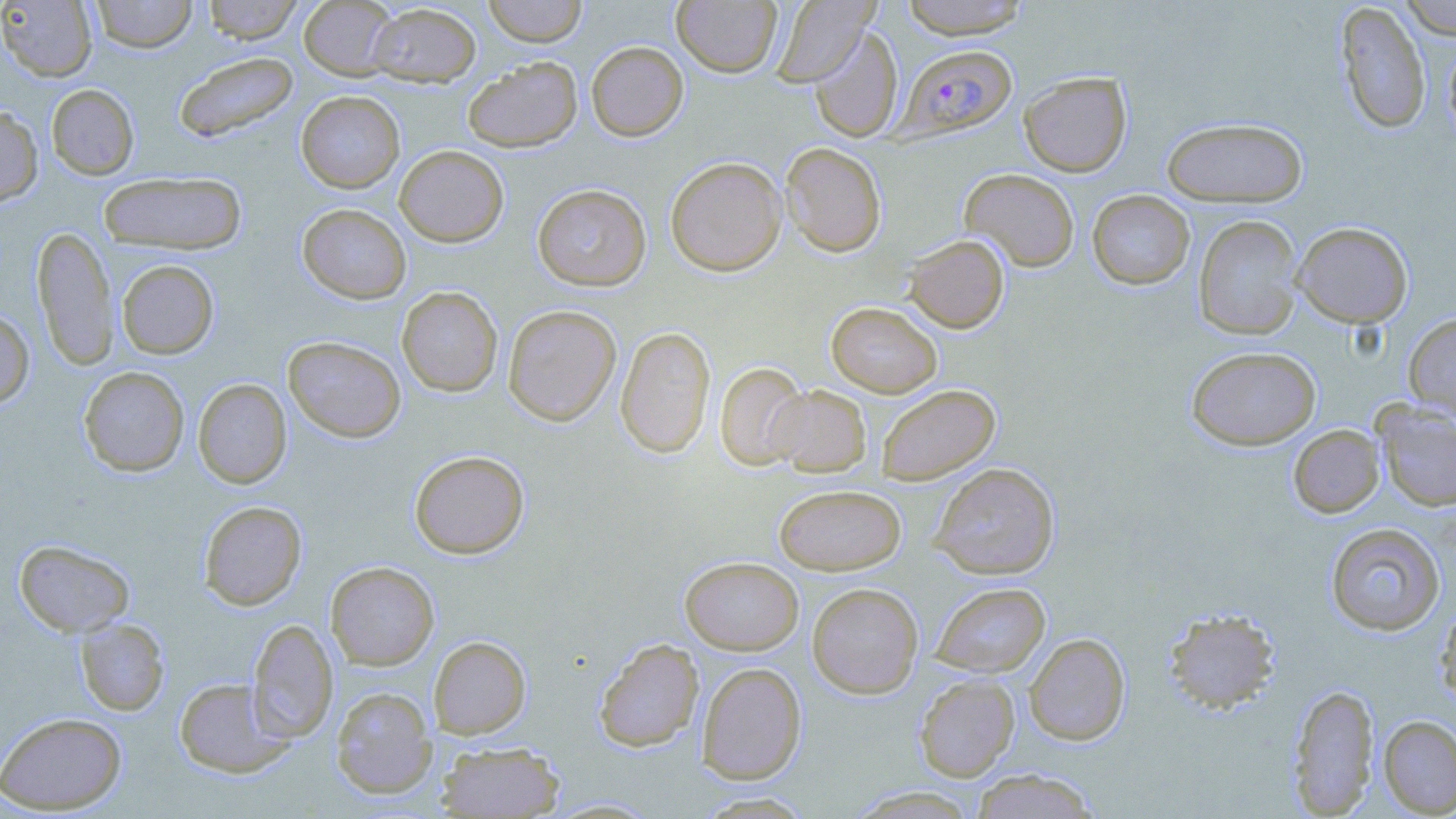
plasmodium_falciparum_infected_red_blood_cell_locations: 'approximate bounding boxes as (x1, y1, x2, y2) in pixels: (895, 44, 1017, 142)'
slide_level_diagnosis: Plasmodium falciparum
stain: May-Grünwald-Giemsa
modality: optical microscopy
field_of_view: one of a larger specimen
uninfected_red_blood_cell_locations: 'approximate bounding boxes as (x1, y1, x2, y2) in pixels: (0, 0, 97, 82), (90, 0, 198, 53), (202, 0, 304, 44), (299, 0, 399, 80), (482, 0, 587, 46), (770, 0, 877, 86), (898, 0, 1031, 39), (1398, 0, 1456, 38), (671, 1, 782, 77), (1335, 1, 1431, 135), (368, 3, 482, 87), (809, 27, 903, 143), (1443, 36, 1456, 145), (586, 41, 688, 141), (173, 51, 299, 144), (463, 57, 583, 152), (1019, 71, 1132, 176), (46, 84, 139, 179), (295, 90, 405, 193), (0, 105, 43, 206), (1161, 117, 1308, 207), (780, 142, 887, 258), (394, 145, 508, 246), (665, 156, 787, 277), (959, 168, 1079, 272), (98, 171, 248, 255), (532, 183, 652, 291), (1087, 190, 1195, 290), (297, 203, 411, 304), (1192, 215, 1303, 340), (1291, 221, 1413, 327), (33, 225, 118, 370), (904, 234, 1009, 333), (117, 259, 219, 359), (397, 286, 503, 397), (826, 301, 942, 397), (502, 304, 622, 426), (0, 308, 34, 410), (1403, 312, 1456, 421), (615, 325, 715, 458), (283, 335, 406, 443), (1186, 346, 1321, 450), (715, 361, 809, 471), (78, 367, 189, 477), (193, 378, 292, 488), (876, 384, 1001, 486), (768, 385, 871, 476), (1373, 400, 1456, 511), (1288, 424, 1385, 518), (409, 450, 529, 559), (929, 462, 1060, 580), (774, 484, 906, 575), (199, 500, 307, 611), (1325, 522, 1446, 636), (15, 540, 134, 637), (680, 556, 803, 655), (326, 561, 439, 670), (807, 582, 924, 698), (930, 582, 1051, 677), (1434, 600, 1456, 710), (1162, 606, 1281, 714), (75, 618, 170, 715), (247, 619, 338, 742), (1024, 632, 1131, 745), (429, 635, 530, 738), (594, 637, 704, 752), (696, 662, 807, 784), (914, 674, 1019, 782), (174, 677, 293, 778), (1288, 683, 1379, 815), (331, 686, 437, 798), (0, 711, 127, 814), (1378, 715, 1456, 817), (435, 741, 565, 818), (969, 769, 1101, 818)'
preparation: thin blood smear
image_size: 1456×819 pixels
magnification: 1000x